State which parasite is depicted.
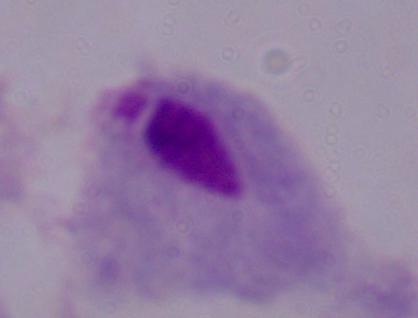

A trichomonad.

1000x magnification. Micrograph.